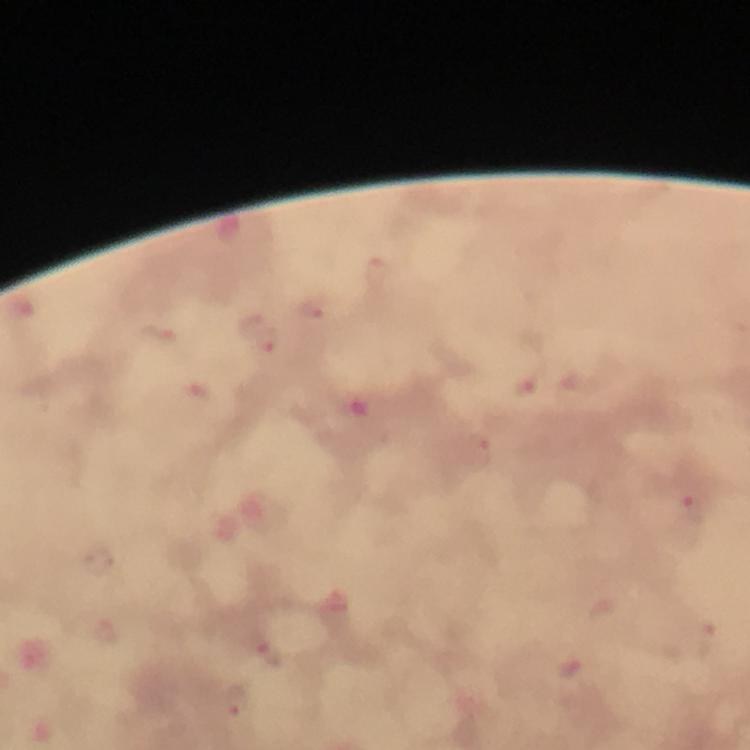

Approximate object centers, in pixels from the top-left corner. Malaria parasite locations: (x=377, y=273), (x=313, y=307), (x=159, y=335), (x=267, y=341), (x=525, y=386), (x=481, y=454), (x=686, y=507), (x=271, y=656), (x=568, y=669), (x=236, y=701). From a diagnostic examination for malaria. Cropped region of a single field of view. Giemsa stain. Photographed with a smartphone mounted on the microscope. Image is 750×750 pixels. Immersion oil was used. 100x magnification. Thick smear.